State the blood parasite species.
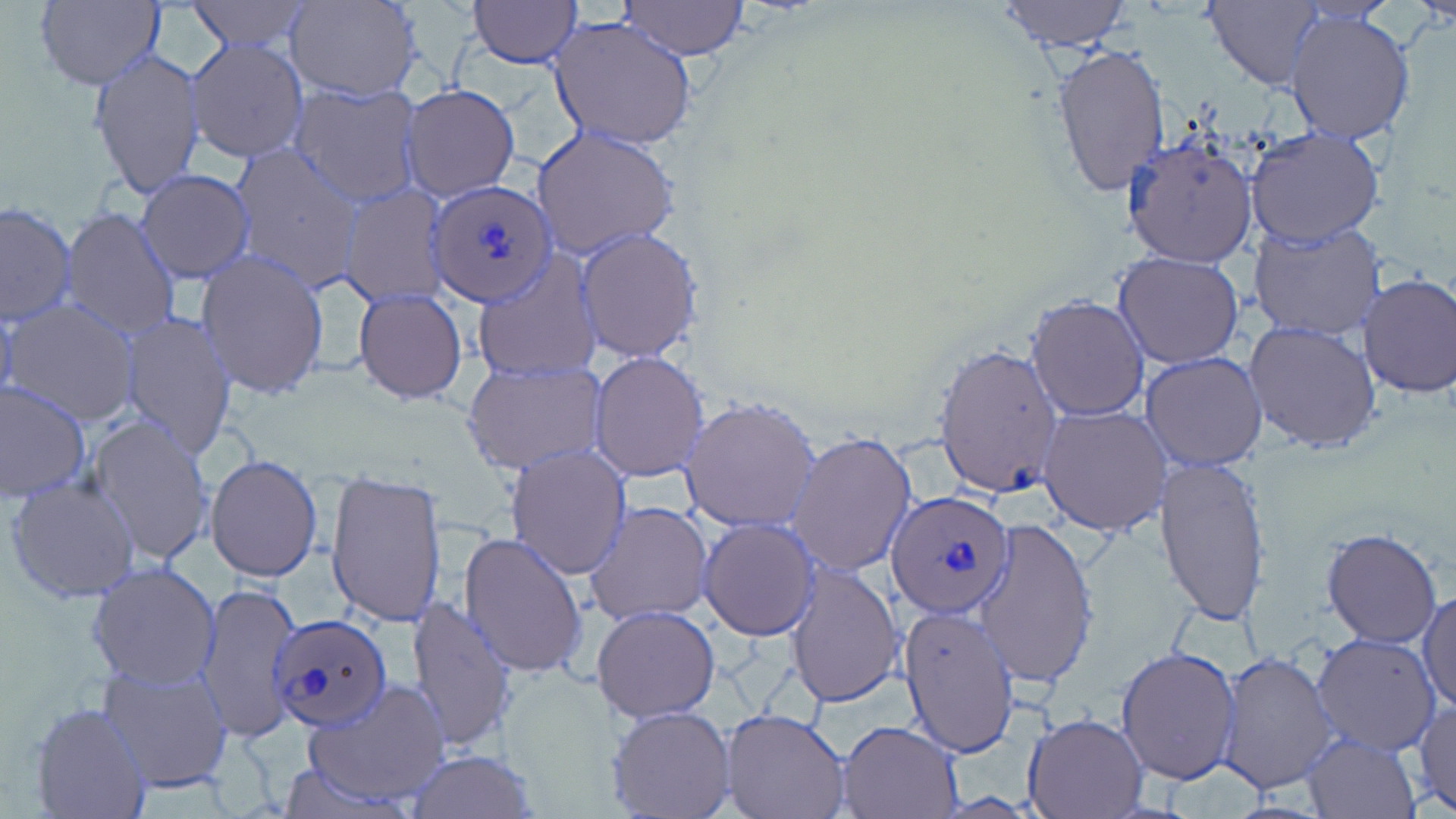

Plasmodium ovale.

uninfected red blood cell locations = approximate bounding boxes as named x1/y1/x2/y2 corners in pixels: (x1=34, y1=0, x2=165, y2=91), (x1=184, y1=0, x2=315, y2=52), (x1=284, y1=0, x2=422, y2=101), (x1=466, y1=0, x2=580, y2=67), (x1=617, y1=0, x2=751, y2=60), (x1=995, y1=0, x2=1132, y2=52), (x1=1207, y1=0, x2=1327, y2=90), (x1=1283, y1=7, x2=1417, y2=145), (x1=548, y1=16, x2=698, y2=150), (x1=186, y1=36, x2=308, y2=164), (x1=1049, y1=42, x2=1170, y2=198), (x1=89, y1=49, x2=204, y2=204), (x1=289, y1=81, x2=423, y2=205), (x1=402, y1=83, x2=520, y2=200), (x1=1243, y1=125, x2=1387, y2=247), (x1=532, y1=126, x2=681, y2=259), (x1=1124, y1=135, x2=1258, y2=270), (x1=231, y1=144, x2=362, y2=291), (x1=136, y1=170, x2=255, y2=281), (x1=338, y1=183, x2=450, y2=308), (x1=0, y1=202, x2=78, y2=326), (x1=61, y1=207, x2=182, y2=340), (x1=1247, y1=218, x2=1388, y2=341), (x1=577, y1=228, x2=703, y2=361), (x1=195, y1=250, x2=330, y2=400), (x1=1113, y1=252, x2=1243, y2=369), (x1=471, y1=254, x2=601, y2=383), (x1=1358, y1=273, x2=1456, y2=398), (x1=352, y1=286, x2=468, y2=403), (x1=1024, y1=294, x2=1151, y2=422), (x1=3, y1=299, x2=138, y2=427), (x1=116, y1=312, x2=238, y2=458), (x1=1245, y1=319, x2=1382, y2=456), (x1=934, y1=342, x2=1061, y2=498), (x1=589, y1=351, x2=710, y2=483), (x1=1141, y1=351, x2=1268, y2=471), (x1=463, y1=358, x2=606, y2=475), (x1=0, y1=380, x2=93, y2=503), (x1=678, y1=396, x2=822, y2=533), (x1=1039, y1=405, x2=1170, y2=535), (x1=85, y1=413, x2=216, y2=569), (x1=787, y1=430, x2=919, y2=577), (x1=506, y1=445, x2=632, y2=581), (x1=205, y1=453, x2=323, y2=581), (x1=1155, y1=454, x2=1271, y2=626), (x1=325, y1=468, x2=447, y2=629), (x1=5, y1=476, x2=141, y2=603), (x1=586, y1=500, x2=714, y2=626), (x1=972, y1=517, x2=1099, y2=690), (x1=699, y1=519, x2=819, y2=639), (x1=1319, y1=528, x2=1442, y2=648), (x1=458, y1=530, x2=587, y2=678), (x1=87, y1=561, x2=222, y2=688), (x1=784, y1=563, x2=904, y2=707), (x1=195, y1=581, x2=302, y2=742), (x1=1418, y1=587, x2=1455, y2=714), (x1=406, y1=595, x2=517, y2=748), (x1=898, y1=603, x2=1021, y2=758), (x1=591, y1=604, x2=718, y2=721), (x1=1311, y1=633, x2=1441, y2=756), (x1=1115, y1=644, x2=1241, y2=785), (x1=1215, y1=651, x2=1338, y2=797), (x1=95, y1=658, x2=236, y2=794), (x1=302, y1=678, x2=452, y2=809), (x1=1412, y1=700, x2=1456, y2=815), (x1=30, y1=701, x2=150, y2=819), (x1=607, y1=706, x2=735, y2=819), (x1=723, y1=709, x2=851, y2=819), (x1=1021, y1=713, x2=1147, y2=818), (x1=839, y1=719, x2=963, y2=818), (x1=1301, y1=732, x2=1419, y2=819), (x1=406, y1=750, x2=537, y2=818)
Plasmodium ovale-infected red blood cell locations = approximate bounding boxes as named x1/y1/x2/y2 corners in pixels: (x1=428, y1=180, x2=554, y2=305), (x1=888, y1=491, x2=1014, y2=616), (x1=266, y1=613, x2=389, y2=735)
preparation = thin blood film
stain = May-Grünwald-Giemsa
image size = 1456×819 pixels
magnification = 1000x
field of view = single
modality = optical microscopy